Comment on the morphology of the erythrocytes.
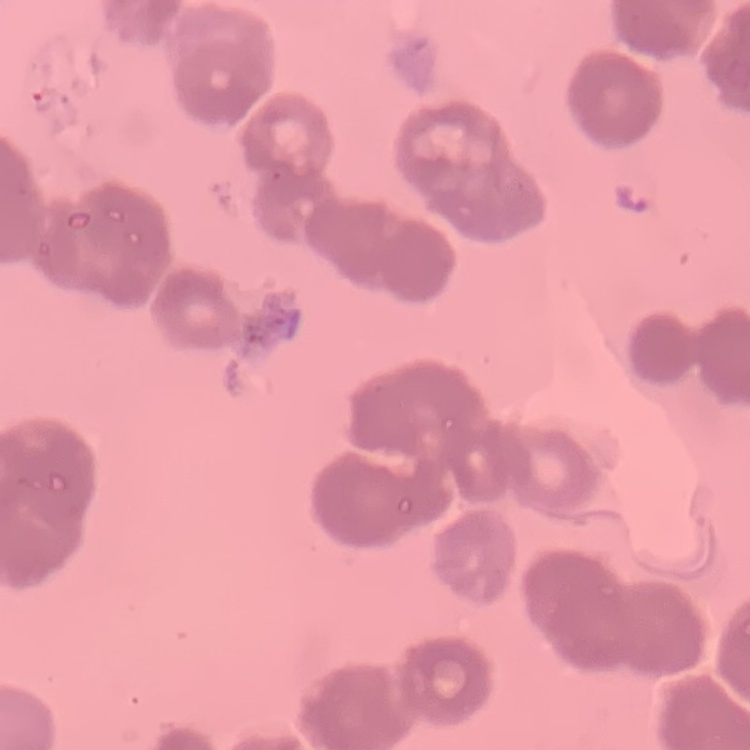
They show rouleaux formation.

One tile cut from a larger photomicrograph. Field's or Giemsa stain. Thin peripheral smear.